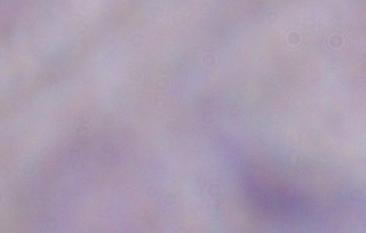
identification = trypanosome
magnification = 1000x
modality = micrograph